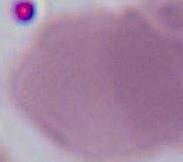
magnification = 1000x
identification = red blood cell
modality = photomicrograph